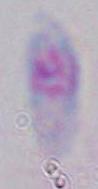

Toxoplasma gondii is seen. Photomicrograph. Captured at 1000x magnification.